Assess this cell for malaria.
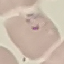
Parasitized.

preparation: thin smear
capture: smartphone camera at the microscope eyepiece
stain: Giemsa
image_type: automatically extracted cell patch, resized to 64 × 64 pixels